Report the malaria status of this cell.
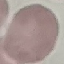

Uninfected.

Thin blood smear. Giemsa stain. Photographed with a smartphone camera at the microscope eyepiece. Cell patch, automatically extracted from a larger field of view and resized to 64 × 64 pixels.